Classify this cell by malaria status.
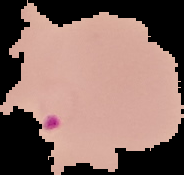

Parasitized.

image size = 184×175 pixels
preparation = thin blood smear
image type = segmented cell region on a black background